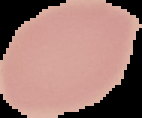

Summary:
  - Result: no Plasmodium parasites seen
  - Image type: cell region segmented out of the field of view; surrounding area masked to black
  - Preparation: thin blood smear
  - Image size: 142×118 pixels